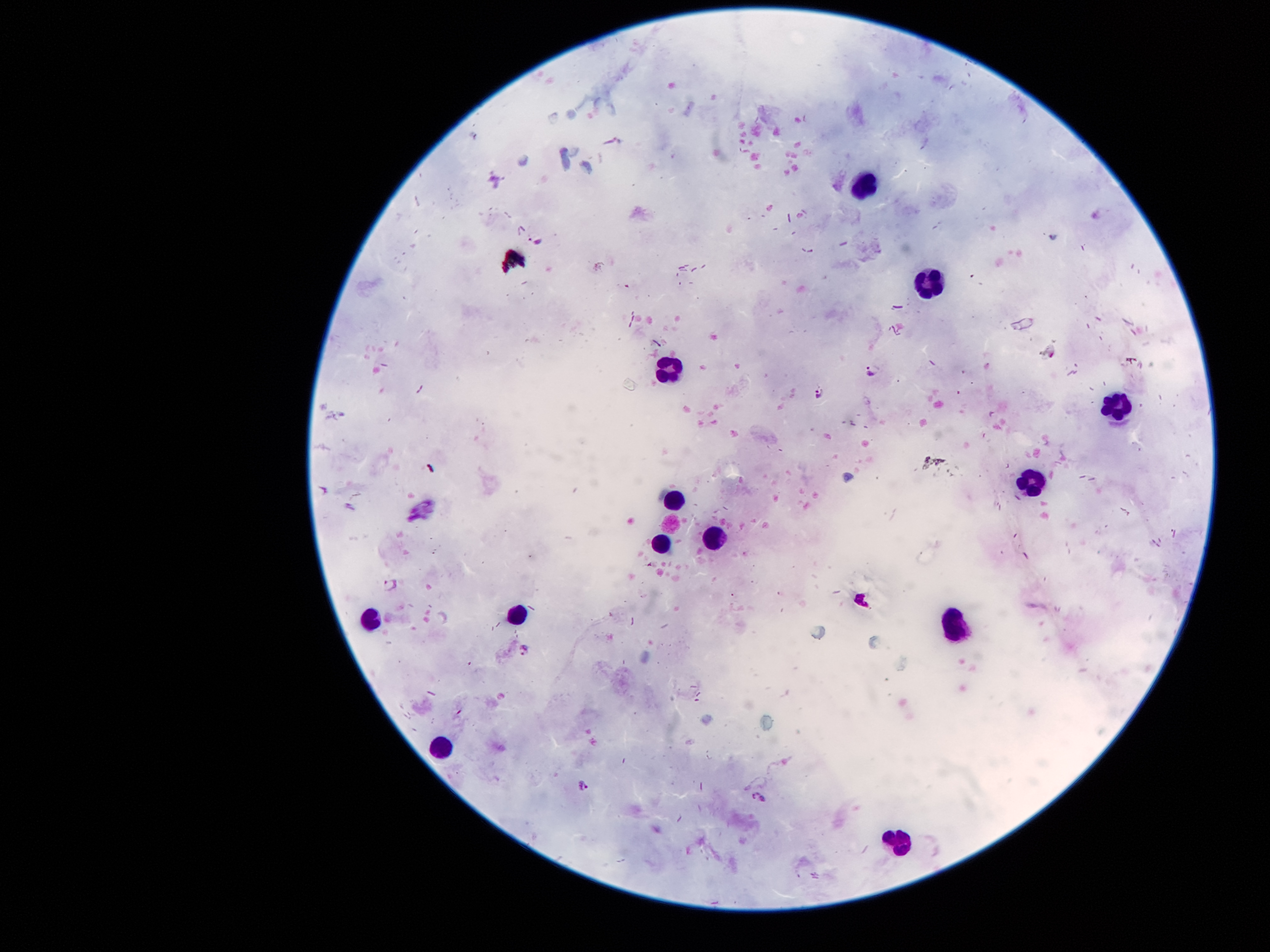
coordinate format = approximate centers as (x, y) in pixels
malaria parasite locations = (537, 238), (873, 370), (818, 394), (390, 585), (524, 651), (583, 785), (761, 795)
leukocyte locations = (866, 182), (927, 290), (662, 367), (1115, 409), (1031, 480), (672, 498), (711, 537), (659, 544), (517, 613), (368, 619), (957, 622), (436, 750), (902, 841)
preparation = thick peripheral-blood smear
stain = Giemsa
capture = smartphone camera through the microscope eyepiece
patient malaria status = positive for Plasmodium falciparum
magnification = 100x
image size = 1270×952 pixels
field of view = one from this slide